Locate and identify every blood parasite.
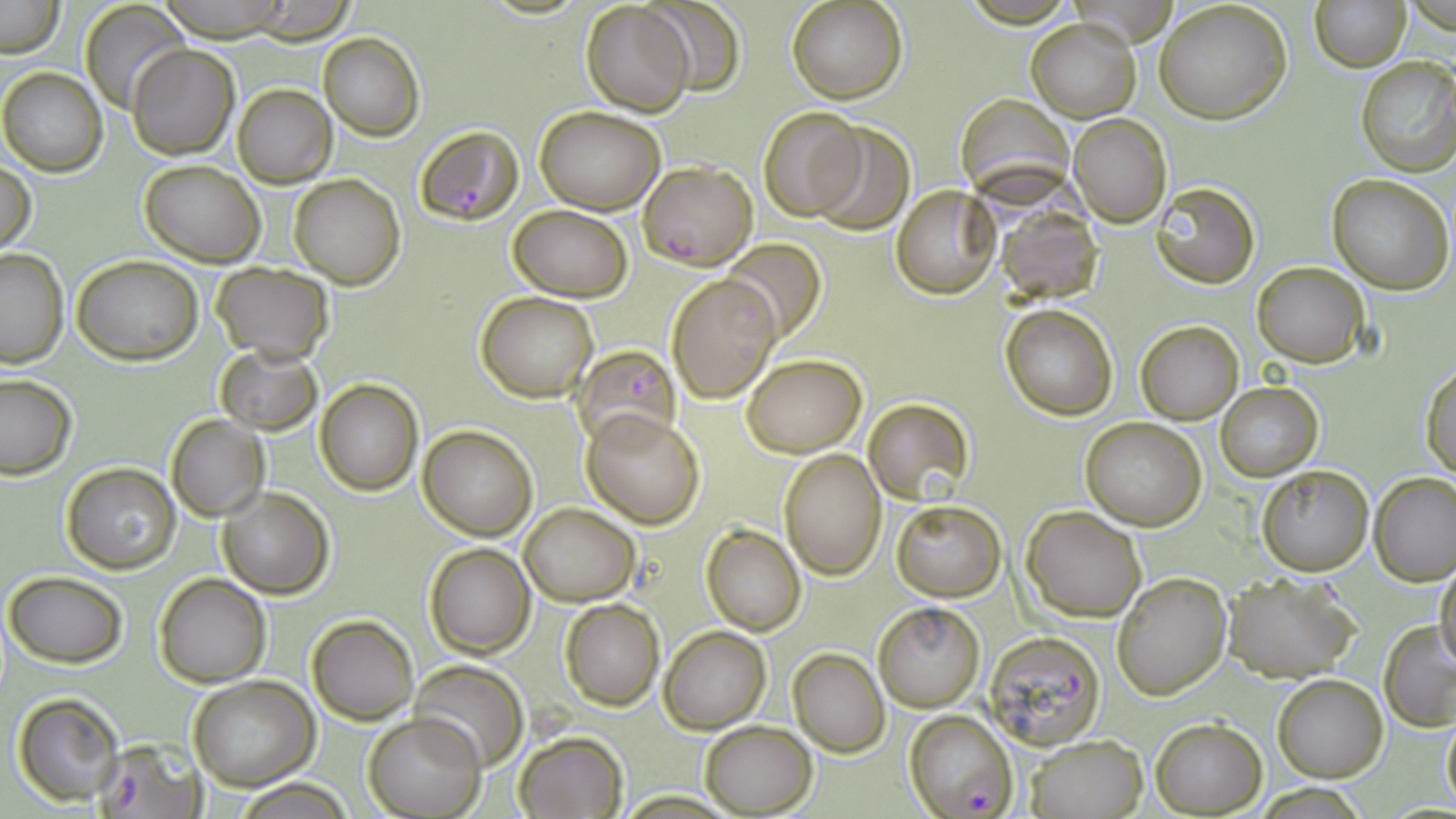
Approximate bounding boxes as (x1,y1)-(x2,y2) corner pairs in pixels.
Plasmodium falciparum-infected red blood cells: (412,125)-(524,227), (639,161)-(757,269), (574,346)-(678,449), (983,631)-(1105,749), (905,711)-(1018,818), (96,741)-(203,817).
No Plasmodium ovale, Plasmodium malariae, Plasmodium vivax, Babesia divergens, or Trypanosoma brucei observed.

Uninfected red blood cell locations: (0,0)-(65,57), (787,0)-(907,104), (1310,0)-(1409,71), (80,1)-(190,115), (154,1)-(296,40), (580,1)-(696,117), (644,1)-(748,96), (1154,2)-(1292,124), (243,4)-(359,41), (1027,19)-(1139,121), (318,32)-(424,141), (126,45)-(239,159), (1355,55)-(1456,176), (1,66)-(106,177), (232,84)-(336,187), (535,106)-(665,214), (757,108)-(866,220), (1070,114)-(1172,227), (807,123)-(915,232), (138,159)-(265,266), (0,160)-(35,253), (289,174)-(405,289), (1327,174)-(1454,294), (1152,181)-(1260,290), (892,184)-(1000,300), (508,205)-(634,300), (998,206)-(1102,303), (721,237)-(827,347), (0,249)-(68,367), (72,254)-(203,365), (1251,262)-(1369,367), (211,263)-(335,361), (666,273)-(780,403), (477,291)-(599,402), (1001,305)-(1116,419), (1135,320)-(1243,424), (215,345)-(323,436), (743,355)-(866,456), (1420,361)-(1455,478), (0,374)-(76,480), (315,379)-(424,496), (1216,383)-(1322,480), (863,398)-(973,506), (583,409)-(706,527), (166,414)-(268,520), (1081,418)-(1206,530), (420,425)-(537,541), (777,448)-(885,581), (61,462)-(181,575), (1256,464)-(1374,577), (1371,473)-(1456,585), (218,487)-(335,598), (891,500)-(1005,600), (519,501)-(639,605), (1021,505)-(1147,621), (701,524)-(806,635), (424,541)-(536,659), (1435,562)-(1456,672), (4,571)-(128,668), (1112,572)-(1231,700), (1222,573)-(1360,682), (155,574)-(271,688), (559,599)-(665,710), (873,603)-(985,711), (307,613)-(418,725), (1379,621)-(1456,730), (660,625)-(772,734), (787,650)-(888,756), (410,660)-(528,771), (187,676)-(317,790), (1272,676)-(1387,782), (12,691)-(124,807), (1441,711)-(1456,810), (363,715)-(484,818), (1151,718)-(1265,816), (699,721)-(816,816), (514,731)-(626,818), (1026,734)-(1147,818), (233,780)-(359,817). Slide-level diagnosis: Plasmodium falciparum. Optical microscopy. May-Grünwald-Giemsa stain. Thin blood smear. Image is 1456×819 pixels. Single field of view. Captured at 1000x magnification.